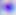
identification = Toxoplasma gondii
magnification = 400x
modality = micrograph